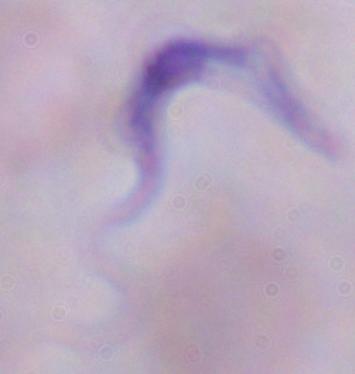
Micrograph. Captured at 1000x magnification. A trypanosome is seen.